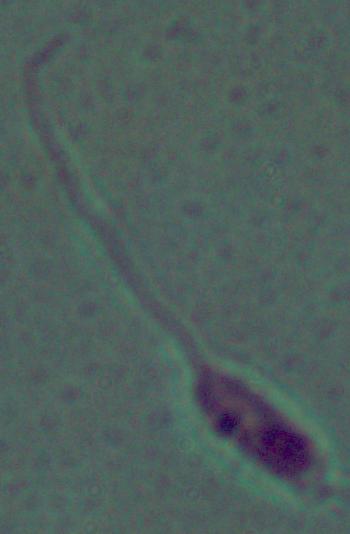

identification = Leishmania
modality = photomicrograph
magnification = 1000x